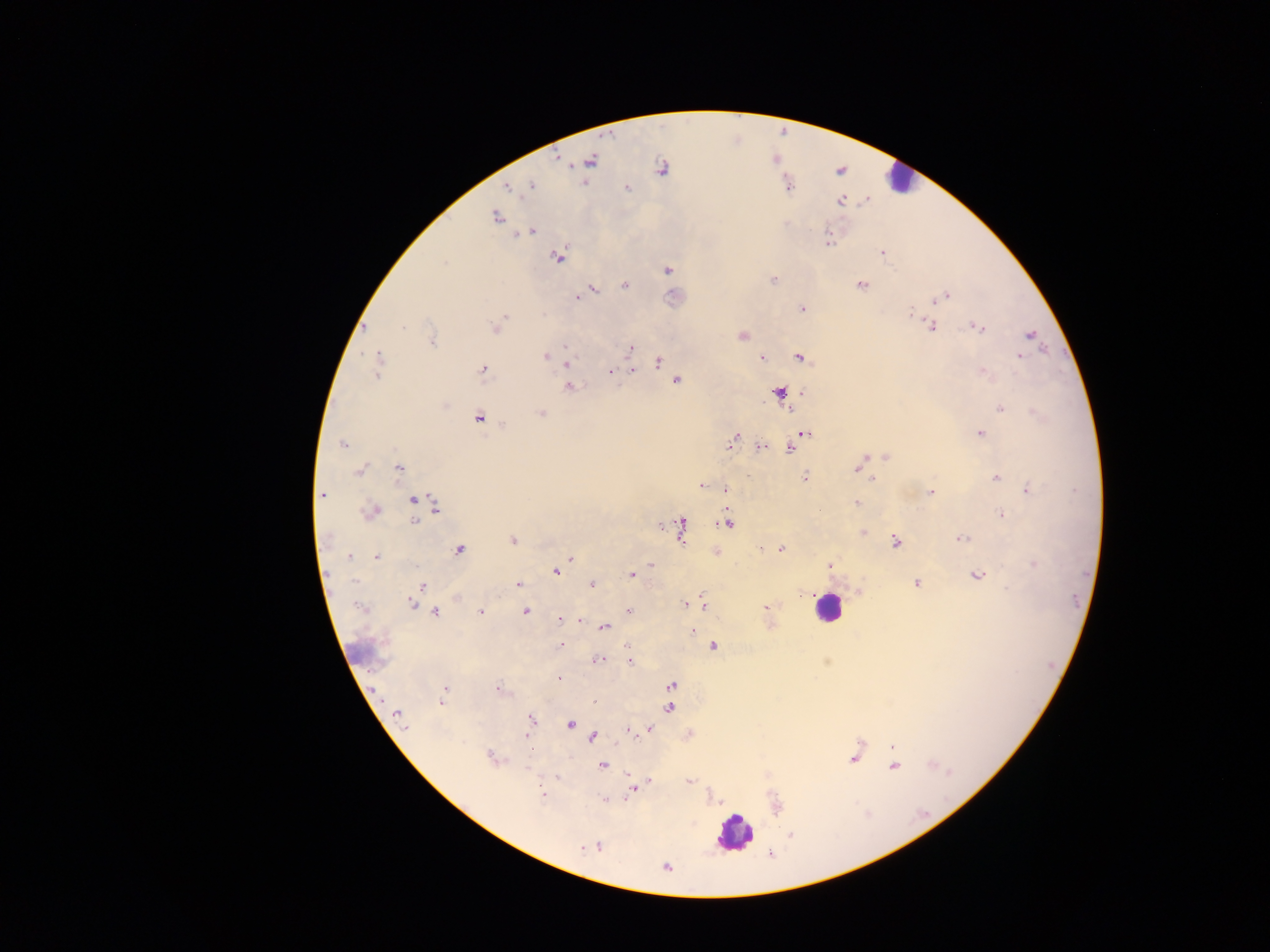

preparation = thick blood film
image size = 1270×952 pixels
country = Ghana
capture = mobile-phone photograph through a microscope
field of view = single
leukocyte locations = approximate centers as {x, y} in pixels: {898, 178}, {827, 608}, {734, 833}
malaria parasite locations = approximate centers as {x, y} in pixels: {591, 161}, {662, 168}, {530, 186}, {509, 187}, {520, 187}, {789, 187}, {627, 189}, {841, 200}, {496, 217}, {532, 231}, {827, 241}, {882, 253}, {558, 256}, {444, 262}, {667, 270}, {773, 280}, {624, 285}, {861, 285}, {591, 290}, {946, 295}, {578, 297}, {938, 298}, {802, 309}, {910, 315}, {502, 319}, {403, 326}, {932, 326}, {365, 327}, {977, 327}, {496, 328}, {742, 335}, {1030, 335}, {431, 340}, {566, 346}, {630, 349}, {545, 356}, {1019, 357}, {762, 358}, {800, 358}, {659, 361}, {568, 362}, {378, 365}, {482, 370}, {632, 371}, {610, 372}, {982, 372}, {677, 381}, {570, 387}, {779, 392}, {802, 393}, {445, 406}, {789, 408}, {1000, 408}, {541, 413}, {479, 417}, {980, 433}, {806, 434}, {733, 438}, {342, 444}, {761, 447}, {789, 448}, {886, 457}, {862, 461}, {399, 468}, {857, 468}, {360, 471}, {805, 477}, {996, 477}, {872, 479}, {701, 485}, {725, 489}, {1028, 490}, {931, 493}, {323, 494}, {413, 501}, {857, 502}, {435, 504}, {374, 511}, {1001, 514}, {414, 521}, {727, 523}, {660, 526}, {682, 530}, {862, 532}, {327, 538}, {963, 538}, {512, 540}, {895, 542}, {762, 549}, {781, 549}, {459, 550}, {350, 556}, {376, 557}, {570, 558}, {651, 564}, {1033, 564}, {828, 565}, {556, 572}, {631, 575}, {977, 575}, {354, 581}, {917, 583}, {591, 584}, {518, 585}, {423, 587}, {801, 594}, {412, 603}, {685, 604}, {703, 604}, {359, 607}, {766, 608}, {525, 611}, {628, 611}, {435, 612}, {480, 612}, {559, 619}, {580, 621}, {604, 627}, {693, 631}, {561, 644}, {713, 646}, {629, 650}, {599, 660}, {629, 660}, {559, 679}, {671, 686}, {445, 688}, {498, 689}, {594, 701}, {441, 702}, {669, 707}, {398, 715}, {532, 719}, {570, 724}, {649, 729}, {628, 730}, {525, 736}, {593, 737}, {892, 747}, {490, 757}, {853, 758}, {602, 765}, {894, 767}, {527, 769}, {557, 777}, {650, 780}, {689, 781}, {631, 792}, {542, 794}, {606, 799}, {791, 834}, {598, 846}, {582, 847}, {665, 867}